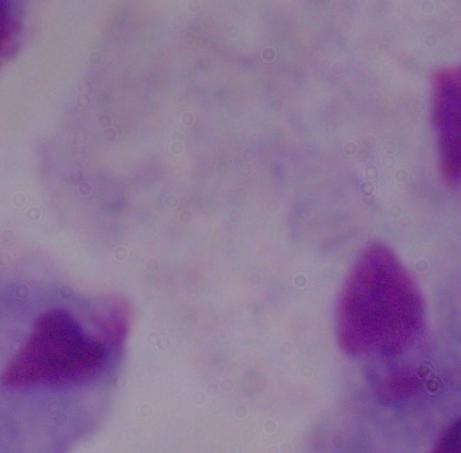
Summary:
  - Magnification: 1000x
  - Identification: trichomonad
  - Modality: micrograph